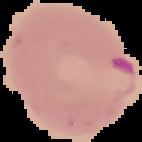

Summary:
  - Image size: 142×142 pixels
  - Image type: segmented cell region on a black background
  - Preparation: thin blood smear
  - Malaria status: parasitized